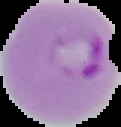

The area outside the segmented cell region is set to black. Image is 121×127 pixels. Malaria status: parasitized. From a thin blood smear.